Identify the parasite.
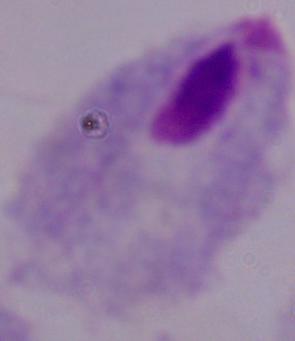

This is a trichomonad.

Micrograph. Captured at 1000x magnification.